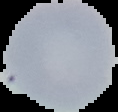

Malaria status: uninfected. Image is 118×112 pixels. From a thin blood film. Cell region segmented out of the field of view; the surrounding area is masked to black.